Report the malaria status of this cell.
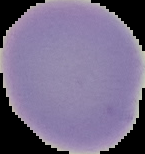
Uninfected.

Summary:
  - Image type: cell region segmented out of the field of view; surrounding area masked to black
  - Preparation: thin blood film
  - Image size: 145×154 pixels